Assess this cell for malaria.
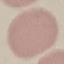
It is uninfected.

Summary:
  - Preparation: thin blood smear
  - Image type: cell patch, automatically extracted from a larger field of view and resized to 64 × 64 pixels
  - Stain: Giemsa
  - Capture: smartphone camera at the microscope eyepiece